Identify the blood parasite species.
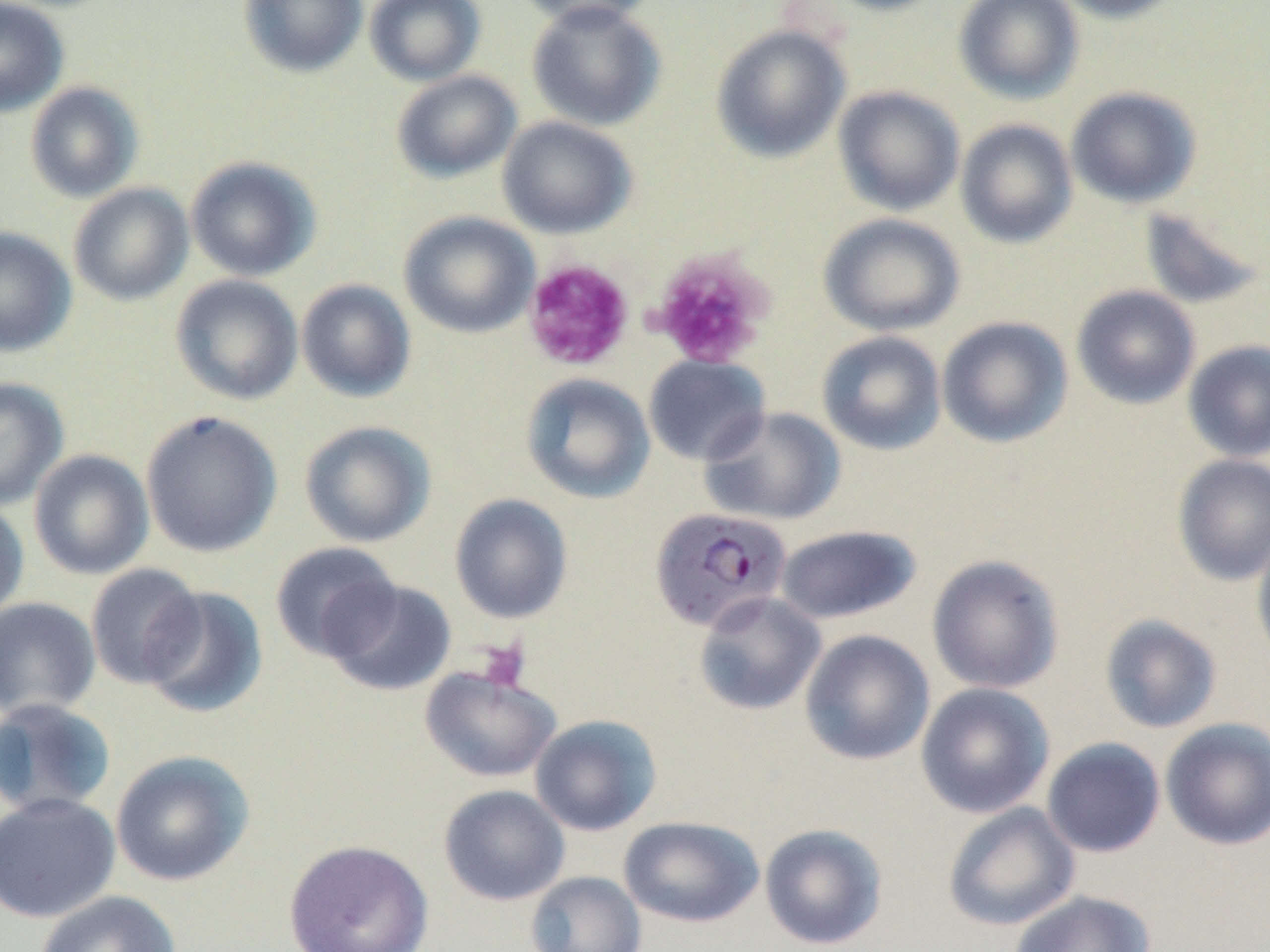

Plasmodium falciparum.

{
  "stain": "May-Grünwald-Giemsa",
  "plasmodium_falciparum_infected_red_blood_cell_locations": "approximate bounding boxes as named x1/y1/x2/y2 corners in pixels: (x1=650, y1=506, x2=791, y2=632)",
  "preparation": "thin blood smear",
  "magnification": "1000x",
  "field_of_view": "one of a larger specimen",
  "platelet_locations": "approximate bounding boxes as named x1/y1/x2/y2 corners in pixels: (x1=649, y1=249, x2=774, y2=369), (x1=522, y1=258, x2=635, y2=371), (x1=475, y1=639, x2=530, y2=691)",
  "modality": "light microscopy",
  "uninfected_red_blood_cell_locations": "approximate bounding boxes as named x1/y1/x2/y2 corners in pixels: (x1=238, y1=0, x2=368, y2=78), (x1=365, y1=0, x2=486, y2=86), (x1=512, y1=0, x2=661, y2=30), (x1=819, y1=0, x2=951, y2=16), (x1=953, y1=0, x2=1084, y2=105), (x1=1046, y1=0, x2=1188, y2=23), (x1=0, y1=1, x2=69, y2=118), (x1=526, y1=1, x2=667, y2=132), (x1=711, y1=24, x2=851, y2=163), (x1=391, y1=70, x2=522, y2=183), (x1=25, y1=81, x2=144, y2=203), (x1=833, y1=86, x2=966, y2=216), (x1=1066, y1=86, x2=1203, y2=209), (x1=497, y1=116, x2=638, y2=239), (x1=955, y1=119, x2=1079, y2=249), (x1=186, y1=156, x2=322, y2=282), (x1=68, y1=183, x2=194, y2=306), (x1=1137, y1=205, x2=1268, y2=310), (x1=399, y1=211, x2=540, y2=338), (x1=819, y1=212, x2=966, y2=337), (x1=0, y1=227, x2=77, y2=356), (x1=170, y1=274, x2=304, y2=406), (x1=296, y1=279, x2=416, y2=403), (x1=1071, y1=285, x2=1201, y2=409), (x1=936, y1=316, x2=1073, y2=448), (x1=816, y1=331, x2=947, y2=455), (x1=1183, y1=339, x2=1270, y2=462), (x1=644, y1=354, x2=770, y2=466), (x1=521, y1=373, x2=655, y2=504), (x1=0, y1=377, x2=69, y2=510), (x1=700, y1=406, x2=845, y2=526), (x1=140, y1=410, x2=283, y2=558), (x1=300, y1=420, x2=436, y2=548), (x1=29, y1=449, x2=154, y2=580), (x1=1172, y1=454, x2=1270, y2=585), (x1=449, y1=494, x2=573, y2=624), (x1=0, y1=499, x2=30, y2=623), (x1=775, y1=524, x2=922, y2=625), (x1=1252, y1=526, x2=1270, y2=671), (x1=270, y1=541, x2=403, y2=663), (x1=927, y1=554, x2=1065, y2=694), (x1=84, y1=563, x2=206, y2=689), (x1=324, y1=579, x2=457, y2=696), (x1=142, y1=586, x2=268, y2=720), (x1=692, y1=591, x2=826, y2=716), (x1=0, y1=597, x2=101, y2=719), (x1=1099, y1=613, x2=1223, y2=734), (x1=799, y1=629, x2=935, y2=765), (x1=420, y1=666, x2=562, y2=783), (x1=915, y1=682, x2=1055, y2=819), (x1=0, y1=697, x2=117, y2=818), (x1=529, y1=714, x2=663, y2=836), (x1=1160, y1=718, x2=1270, y2=850), (x1=1041, y1=737, x2=1166, y2=857), (x1=110, y1=750, x2=255, y2=887), (x1=438, y1=784, x2=570, y2=905), (x1=0, y1=792, x2=121, y2=923), (x1=942, y1=802, x2=1080, y2=931), (x1=619, y1=816, x2=765, y2=927), (x1=759, y1=823, x2=888, y2=950), (x1=283, y1=839, x2=434, y2=952), (x1=525, y1=871, x2=647, y2=952), (x1=34, y1=890, x2=181, y2=952), (x1=1008, y1=890, x2=1155, y2=952)",
  "image_size": "1270×952 pixels"
}